Locate every blood parasite and identify its species.
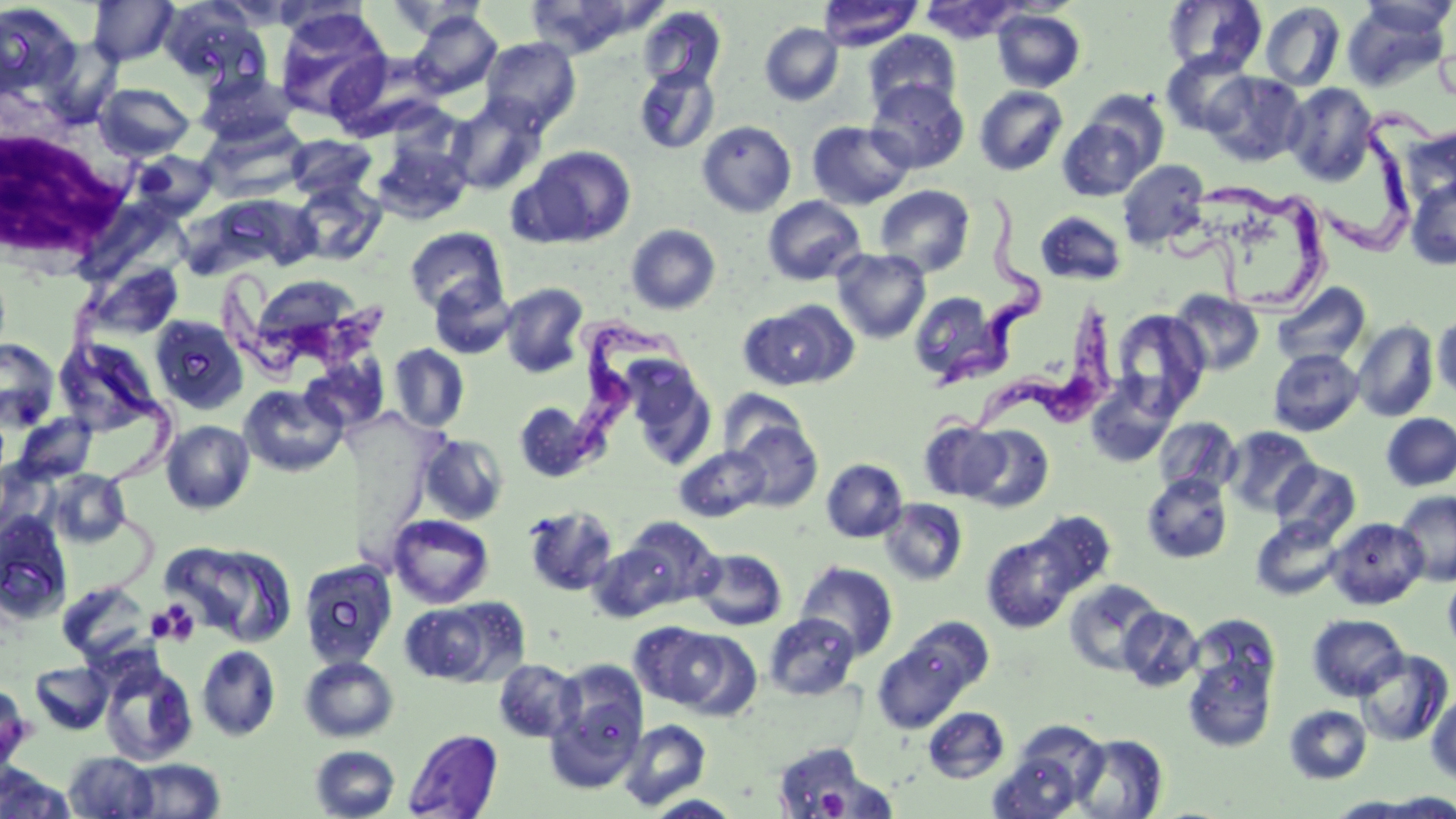
Approximate bounding boxes as (x1,y1)-(x2,y2) corner pairs in pixels.
Trypanosoma brucei: (1322,108)-(1440,261), (1165,178)-(1334,313), (941,196)-(1044,393), (222,270)-(399,385), (942,300)-(1121,439), (570,310)-(697,470).
No Plasmodium falciparum, Plasmodium ovale, Plasmodium malariae, Plasmodium vivax, or Babesia divergens observed.

slide-level diagnosis = Trypanosoma brucei
magnification = 1000x
image size = 1456×819 pixels
stain = May-Grünwald-Giemsa
field of view = one of a larger specimen
white blood cell locations = approximate bounding boxes as (x1,y1)-(x2,y2) corner pairs in pixels: (2,104)-(140,265)
modality = optical microscopy
platelet locations (subset) = approximate bounding boxes as (x1,y1)-(x2,y2) corner pairs in pixels: (150,602)-(200,646), (815,788)-(849,817)
preparation = thin blood smear
uninfected red blood cell locations (subset) = approximate bounding boxes as (x1,y1)-(x2,y2) corner pairs in pixels: (88,0)-(178,66), (159,0)-(267,88), (818,0)-(922,51), (1163,0)-(1267,76), (1357,0)-(1456,40), (272,1)-(371,42), (386,1)-(492,40), (525,1)-(647,57), (920,1)-(1023,44), (1260,2)-(1346,91), (1343,2)-(1451,91), (0,3)-(81,100), (637,7)-(726,92), (274,8)-(392,121), (992,9)-(1085,92), (408,10)-(502,99), (760,23)-(843,106), (864,29)-(961,116), (38,37)-(124,128), (479,37)-(581,133), (1161,51)-(1256,136), (634,66)-(720,155), (196,69)-(300,147), (1204,71)-(1306,167), (866,79)-(969,174), (95,83)-(195,160), (1284,83)-(1378,185), (974,86)-(1068,176), (1077,88)-(1169,180), (445,97)-(548,196), (1058,116)-(1155,201), (696,120)-(796,217), (806,121)-(915,209), (1404,125)-(1456,210), (286,134)-(377,201), (371,138)-(473,225), (515,145)-(637,247), (132,150)-(218,220), (1117,160)-(1209,250), (1406,177)-(1456,269), (292,181)-(387,267), (874,184)-(975,277), (763,196)-(866,286), (1035,210)-(1127,286), (625,223)-(721,315), (404,227)-(509,318), (831,248)-(931,343), (83,261)-(185,340), (427,279)-(516,360), (498,282)-(590,378), (1271,282)-(1372,370), (1169,289)-(1265,377), (909,291)-(1004,388), (739,301)-(854,391), (1110,308)-(1210,416), (1432,310)-(1456,402), (150,315)-(248,414), (1352,320)-(1439,422), (54,337)-(160,435), (0,338)-(59,432), (389,344)-(470,432), (1268,348)-(1364,436), (300,354)-(390,434), (624,358)-(716,469), (1085,374)-(1180,469), (239,384)-(347,477), (719,387)-(811,466), (513,400)-(601,483), (1381,413)-(1456,491), (13,414)-(98,483), (1153,417)-(1241,498), (729,418)-(823,512), (161,420)-(255,514), (919,420)-(1010,502), (961,425)-(1054,513), (1224,426)-(1319,517), (419,432)-(509,526), (673,445)-(771,522), (821,458)-(907,542), (0,459)-(56,539), (1270,460)-(1360,544), (49,469)-(130,547), (1142,473)-(1233,563), (1395,490)-(1456,586), (878,498)-(968,586), (521,505)-(619,596), (1018,511)-(1116,604), (0,513)-(73,624), (388,514)-(494,609), (617,516)-(722,611), (1251,517)-(1345,601), (1326,517)-(1428,609), (982,522)-(1091,633), (163,539)-(297,647), (588,540)-(681,623), (693,548)-(787,631), (299,558)-(398,670), (794,562)-(899,661), (1443,569)-(1456,658), (1064,578)-(1164,676), (56,581)-(154,664), (398,599)-(520,687), (1118,606)-(1204,692), (763,613)-(861,701), (1187,613)-(1280,704), (1307,614)-(1408,701), (639,623)-(757,717), (873,629)-(978,733), (196,645)-(281,741), (1183,648)-(1277,753), (1355,648)-(1452,747), (299,656)-(398,742), (494,659)-(582,743), (30,661)-(112,734), (100,661)-(198,765), (1426,691)-(1456,784), (1285,705)-(1372,784), (923,707)-(1010,783), (618,719)-(711,810), (404,729)-(503,818), (988,731)-(1103,818), (1070,733)-(1169,818), (766,739)-(887,816), (309,745)-(400,819), (64,751)-(158,818), (123,758)-(225,817), (0,764)-(75,817), (1369,793)-(1456,818), (644,794)-(743,818), (1327,796)-(1429,817)